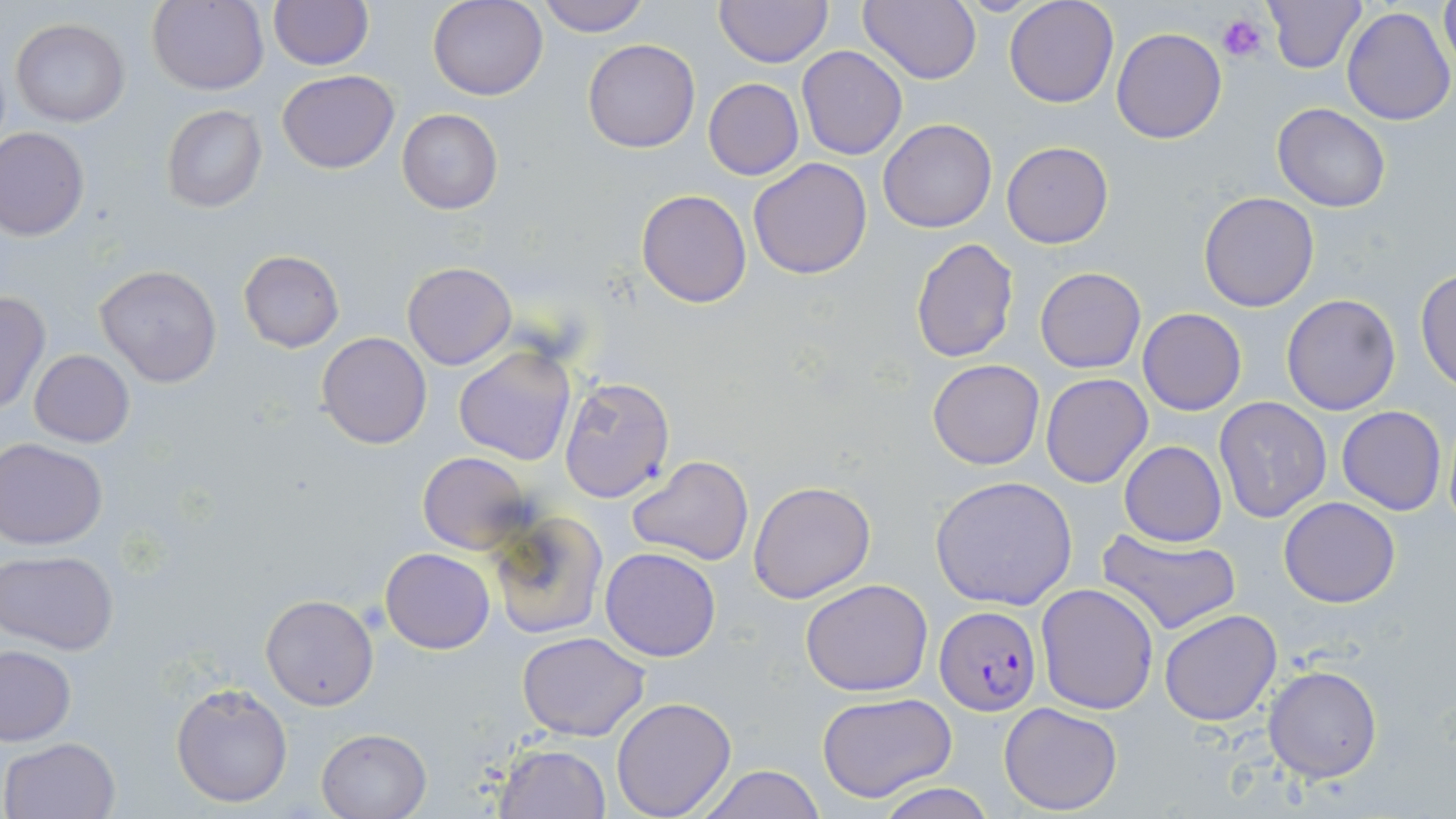
Summary:
  - Coordinate format: approximate bounding boxes as (x1,y1)-(x2,y2) corner pairs in pixels
  - Plasmodium falciparum-infected red blood cell locations: (934,606)-(1041,715)
  - Platelet locations: (1217,13)-(1268,65)
  - Uninfected red blood cell locations: (428,0)-(546,101), (533,0)-(651,37), (713,0)-(834,67), (860,0)-(982,84), (1004,0)-(1118,108), (1266,0)-(1366,73), (1440,0)-(1456,72), (148,1)-(269,95), (268,1)-(374,69), (1340,7)-(1455,127), (10,18)-(129,127), (1112,27)-(1227,144), (582,39)-(700,153), (795,46)-(909,161), (277,69)-(400,174), (702,78)-(803,180), (1272,103)-(1391,211), (162,104)-(267,213), (397,109)-(503,215), (879,119)-(997,233), (0,127)-(89,240), (1002,140)-(1113,249), (747,158)-(873,279), (637,189)-(751,308), (1198,191)-(1321,312), (910,238)-(1019,362), (238,251)-(344,352), (402,261)-(516,370), (94,265)-(222,388), (1035,267)-(1145,373), (1416,267)-(1456,394), (0,291)-(48,413), (1282,293)-(1401,414), (1137,308)-(1247,415), (316,332)-(432,449), (453,345)-(577,466), (28,350)-(135,447), (928,358)-(1045,470), (1041,374)-(1152,488), (557,375)-(674,504), (1212,396)-(1332,524), (1336,406)-(1447,516), (0,437)-(109,549), (1119,441)-(1226,547), (417,451)-(533,554), (625,456)-(753,567), (931,475)-(1079,611), (748,481)-(876,603), (1279,496)-(1400,607), (484,510)-(608,640), (1097,529)-(1244,637), (601,547)-(721,662), (381,548)-(493,654), (1,549)-(119,655), (800,579)-(933,696), (1035,584)-(1159,716), (260,594)-(379,710), (1159,609)-(1282,725), (517,631)-(649,741), (1,645)-(76,745), (1263,664)-(1381,783), (171,683)-(292,807), (818,693)-(956,804), (611,697)-(737,819), (999,703)-(1123,815), (315,727)-(432,819), (3,736)-(121,819), (491,742)-(613,818), (695,766)-(826,819), (875,783)-(994,819)
  - Slide-level diagnosis: Plasmodium falciparum
  - Field of view: single
  - Image size: 1456×819 pixels
  - Magnification: 1000x
  - Modality: light microscopy
  - Preparation: thin blood film
  - Stain: May-Grünwald-Giemsa